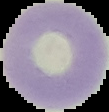

image_type: segmented cell region on a black background
preparation: thin blood film
image_size: 109×112 pixels
malaria_status: uninfected